Outline each uninfected red blood cell.
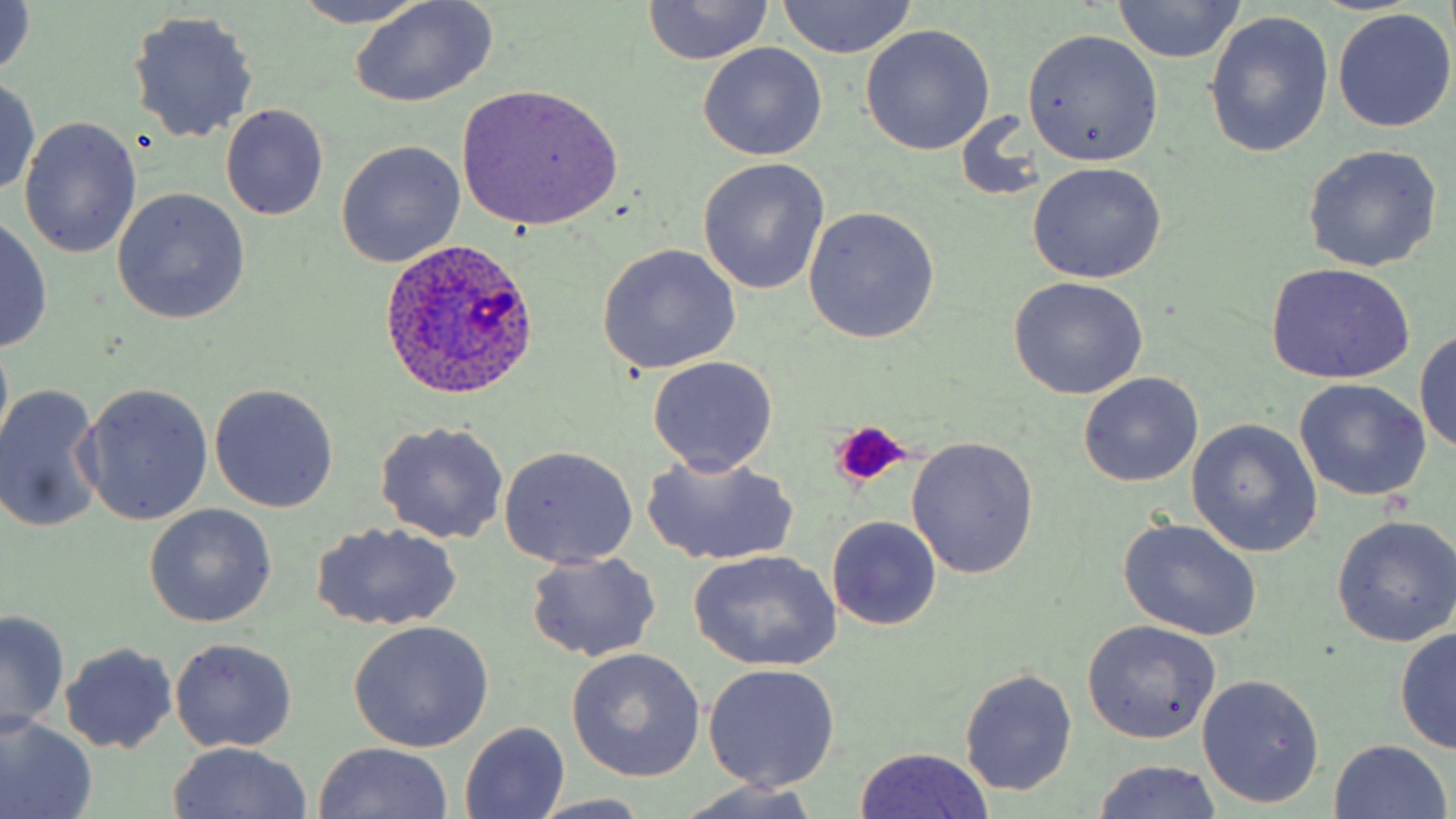
Approximate bounding boxes as named x1/y1/x2/y2 corners in pixels.
Uninfected red blood cells: (x1=0, y1=0, x2=36, y2=78), (x1=641, y1=0, x2=773, y2=66), (x1=291, y1=1, x2=431, y2=28), (x1=350, y1=1, x2=497, y2=107), (x1=1110, y1=1, x2=1245, y2=64), (x1=775, y1=2, x2=918, y2=57), (x1=1332, y1=9, x2=1456, y2=133), (x1=127, y1=10, x2=259, y2=144), (x1=1203, y1=11, x2=1334, y2=158), (x1=860, y1=25, x2=993, y2=154), (x1=1022, y1=28, x2=1165, y2=166), (x1=698, y1=42, x2=827, y2=162), (x1=0, y1=75, x2=41, y2=196), (x1=455, y1=83, x2=624, y2=232), (x1=221, y1=105, x2=329, y2=220), (x1=19, y1=118, x2=143, y2=257), (x1=336, y1=140, x2=466, y2=267), (x1=1303, y1=144, x2=1443, y2=272), (x1=698, y1=160, x2=830, y2=294), (x1=1026, y1=162, x2=1167, y2=283), (x1=111, y1=188, x2=250, y2=325), (x1=804, y1=206, x2=939, y2=343), (x1=0, y1=213, x2=53, y2=354), (x1=596, y1=244, x2=741, y2=374), (x1=1265, y1=263, x2=1415, y2=384), (x1=1008, y1=277, x2=1149, y2=399), (x1=1415, y1=330, x2=1455, y2=454), (x1=648, y1=357, x2=779, y2=476), (x1=1077, y1=372, x2=1204, y2=488), (x1=1293, y1=379, x2=1430, y2=501), (x1=210, y1=382, x2=339, y2=513), (x1=0, y1=383, x2=104, y2=534), (x1=80, y1=383, x2=213, y2=526), (x1=375, y1=420, x2=510, y2=544), (x1=1187, y1=420, x2=1320, y2=557), (x1=906, y1=436, x2=1039, y2=581), (x1=499, y1=446, x2=638, y2=568), (x1=642, y1=454, x2=799, y2=565), (x1=144, y1=504, x2=276, y2=628), (x1=826, y1=516, x2=942, y2=632), (x1=1117, y1=517, x2=1264, y2=641), (x1=1331, y1=517, x2=1456, y2=648), (x1=314, y1=522, x2=460, y2=632), (x1=689, y1=550, x2=843, y2=672), (x1=526, y1=552, x2=661, y2=662), (x1=1, y1=609, x2=69, y2=732), (x1=1082, y1=619, x2=1221, y2=744), (x1=348, y1=621, x2=494, y2=752), (x1=1394, y1=628, x2=1456, y2=755), (x1=168, y1=637, x2=297, y2=752), (x1=59, y1=642, x2=178, y2=755), (x1=566, y1=648, x2=705, y2=781), (x1=703, y1=663, x2=841, y2=792), (x1=958, y1=668, x2=1078, y2=797), (x1=1197, y1=673, x2=1325, y2=809), (x1=0, y1=715, x2=97, y2=819), (x1=459, y1=722, x2=569, y2=816), (x1=1329, y1=739, x2=1451, y2=818), (x1=314, y1=742, x2=453, y2=818), (x1=168, y1=743, x2=313, y2=818), (x1=853, y1=746, x2=997, y2=819), (x1=1092, y1=760, x2=1225, y2=818), (x1=672, y1=783, x2=831, y2=819), (x1=529, y1=794, x2=655, y2=816).

Platelet locations: (x1=832, y1=420, x2=912, y2=488). Plasmodium ovale-infected red blood cell locations: (x1=380, y1=238, x2=543, y2=405). Slide-level diagnosis: Plasmodium ovale. Thin blood film. Light microscopy. One field of a larger specimen. Image is 1456×819 pixels. Captured at 1000x magnification. May-Grünwald-Giemsa-stained preparation.